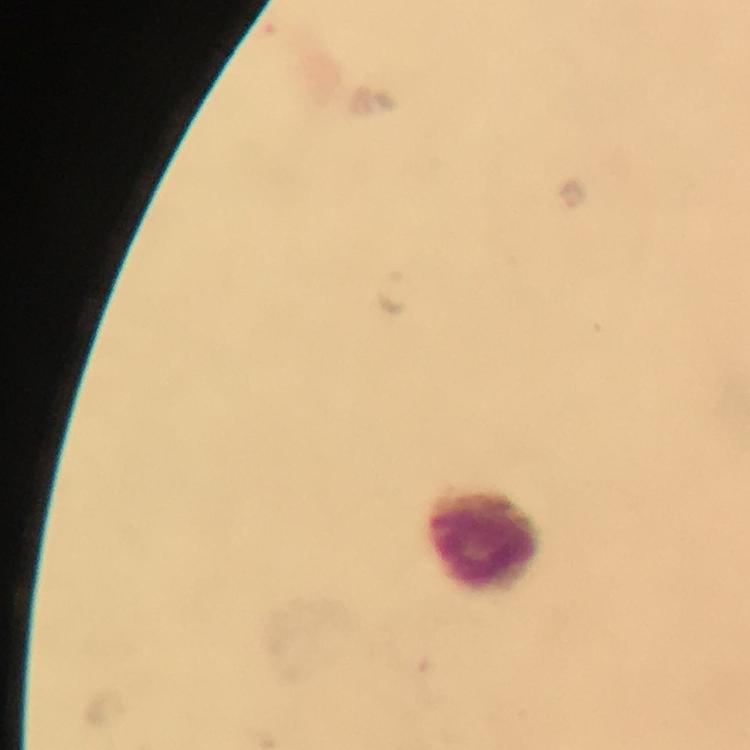

Approximate object centers, in pixels from the top-left corner. Leukocyte locations: (x=482, y=535). Plasmodium parasite locations: (x=571, y=194), (x=395, y=291). 100x magnification. Image is 750×750 pixels. Thick blood film. A crop from one field of view. From a malaria diagnostic workup. Immersion oil applied. Giemsa-stained preparation. Photographed through the microscope with a smartphone camera.